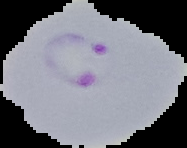
Summary:
  - Image size: 187×148 pixels
  - Preparation: thin blood smear
  - Malaria status: parasitized
  - Image type: cell region segmented out of the field of view; surrounding area masked to black